Outline each Plasmodium falciparum-infected red blood cell.
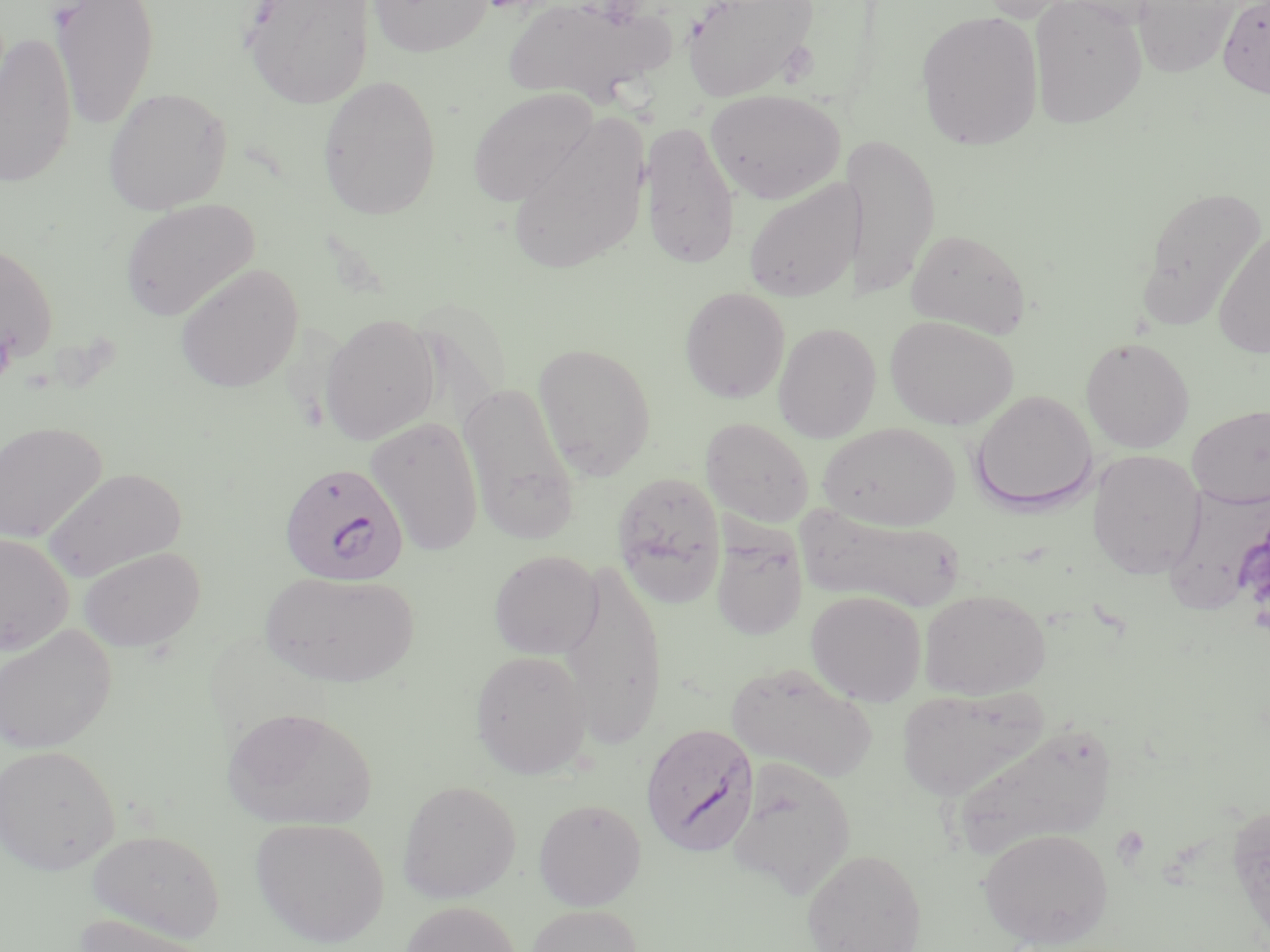
Approximate bounding boxes as (x1,y1)-(x2,y2) corner pairs in pixels.
Plasmodium falciparum-infected red blood cells: (278,461)-(409,585), (641,723)-(759,857).

Summary:
  - Platelet locations: (0,326)-(16,384)
  - Uninfected red blood cell locations: (49,0)-(159,130), (240,0)-(375,108), (368,0)-(494,57), (502,0)-(668,106), (681,0)-(820,102), (974,0)-(1082,23), (1029,0)-(1147,129), (1217,0)-(1270,98), (1133,1)-(1241,76), (916,10)-(1044,151), (0,32)-(78,189), (317,74)-(442,220), (102,86)-(232,214), (467,87)-(599,207), (705,89)-(845,204), (506,118)-(651,277), (639,119)-(740,271), (841,132)-(940,301), (743,177)-(860,303), (1137,184)-(1267,328), (119,197)-(260,321), (906,227)-(1031,338), (1213,227)-(1270,359), (0,241)-(59,365), (174,262)-(304,393), (679,286)-(790,403), (321,313)-(439,444), (885,315)-(1019,430), (773,322)-(882,442), (1081,336)-(1195,453), (533,342)-(656,480), (459,380)-(579,544), (971,390)-(1097,514), (1187,404)-(1270,508), (366,415)-(485,558), (700,417)-(814,527), (0,420)-(107,543), (819,422)-(960,530), (1087,449)-(1205,579), (42,467)-(186,581), (612,471)-(725,605), (1163,483)-(1269,615), (800,507)-(966,612), (710,526)-(808,640), (0,534)-(74,656), (79,546)-(205,653), (489,550)-(602,659), (560,557)-(667,749), (261,570)-(418,688), (918,588)-(1051,700), (806,590)-(927,705), (0,624)-(117,754), (470,649)-(592,779), (726,661)-(878,782), (896,686)-(1048,800), (221,706)-(377,830), (946,721)-(1117,861), (0,744)-(120,874), (727,757)-(856,898), (398,780)-(521,903), (533,798)-(646,910), (1227,801)-(1270,943), (250,817)-(390,947), (979,827)-(1113,948), (85,829)-(226,942), (801,848)-(927,952), (399,901)-(521,952), (526,905)-(643,952), (74,915)-(220,952)
  - Slide-level diagnosis: Plasmodium falciparum
  - Modality: light microscopy
  - Stain: May-Grünwald-Giemsa
  - Preparation: thin blood smear
  - Magnification: 1000x
  - Field of view: one of a larger specimen
  - Image size: 1270×952 pixels